Comment on the morphology of the erythrocytes.
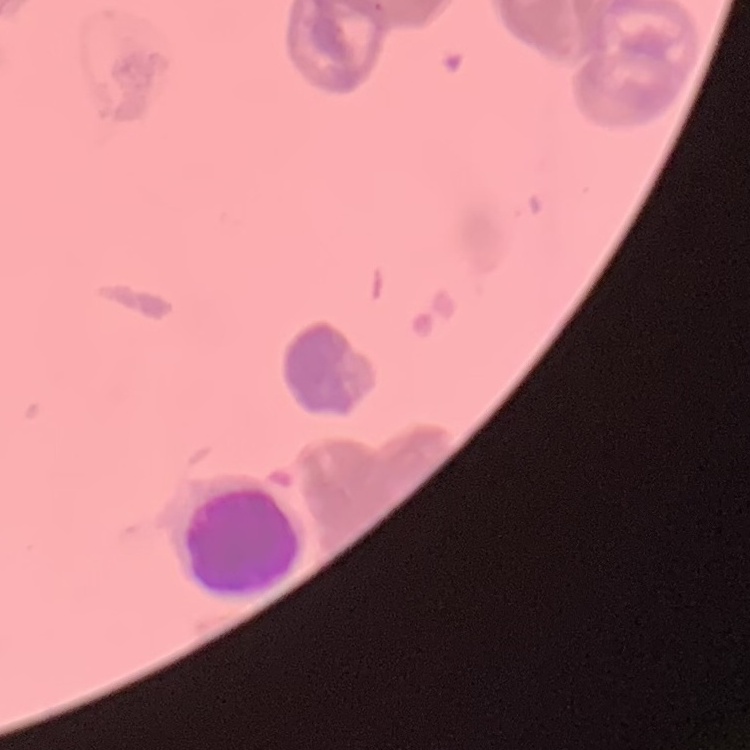

They show rouleaux formation.

Summary:
  - Preparation: thin blood smear
  - Stain: Field's or Giemsa
  - Image type: one tile cut from a larger photomicrograph